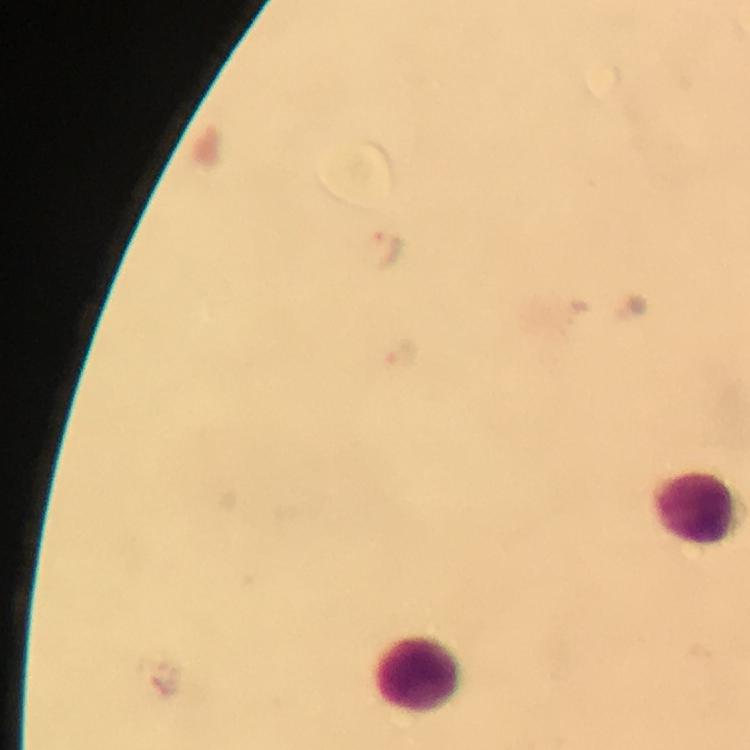

{
  "capture": "smartphone mounted on the microscope",
  "cropped_from": "one field of view",
  "context": "from a malaria diagnostic workup",
  "leukocyte_locations": "approximate centers as {x, y} in pixels: {694, 508}, {419, 674}",
  "immersion_oil": "used",
  "image_size": "750×750 pixels",
  "stain": "Giemsa",
  "magnification": "100x",
  "preparation": "thick blood smear",
  "plasmodium_parasite_locations": "approximate centers as {x, y} in pixels: {384, 250}, {404, 353}"
}